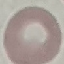

result: no malaria parasites detected
capture: smartphone through the microscope eyepiece
stain: Giemsa
image_type: automatically extracted cell patch, resized to 64 × 64 pixels
preparation: thin blood smear